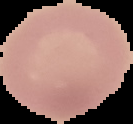

image_type: segmented cell region on a black background
image_size: 133×124 pixels
preparation: thin blood smear
result: negative for malaria parasites